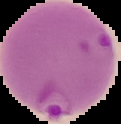

Malaria status: parasitized. Cell region segmented out of the field of view; the surrounding area is masked to black. From a thin blood film. Image is 121×124 pixels.